Classify this cell by malaria status.
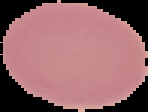
It is uninfected.

Summary:
  - Image size: 148×112 pixels
  - Preparation: thin blood smear
  - Image type: segmented cell region on a black background